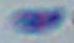
Toxoplasma gondii is shown. Captured at 1000x magnification. Photomicrograph.